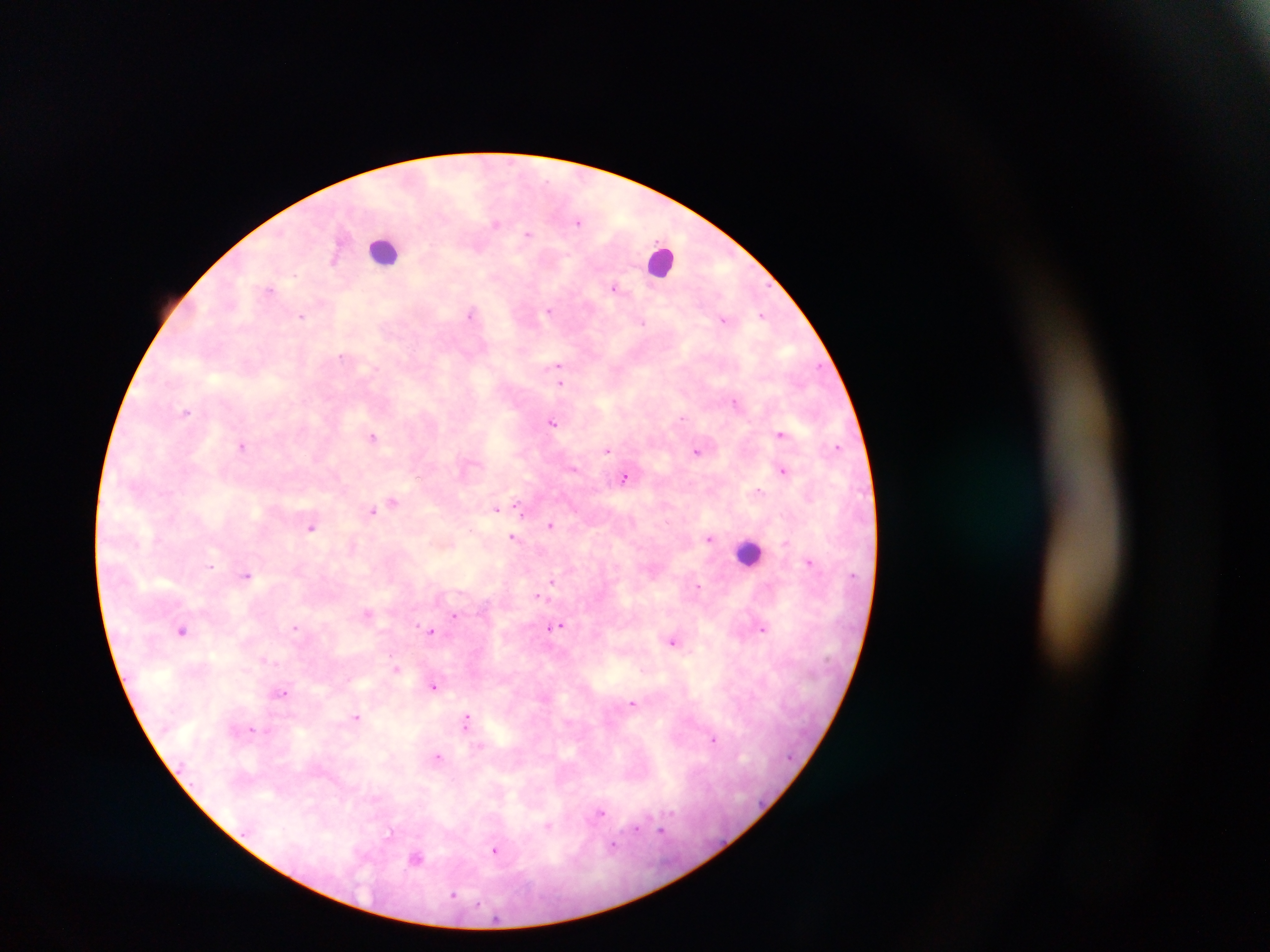 Approximate centers as (x, y) in pixels. Leukocyte locations: (384, 250), (663, 261), (748, 552). Plasmodium parasite locations: (579, 222), (495, 224), (528, 234), (479, 248), (333, 258), (614, 287), (270, 288), (549, 310), (471, 314), (762, 315), (302, 317), (724, 320), (643, 323), (342, 356), (558, 365), (561, 384), (735, 402), (186, 413), (682, 418), (552, 422), (780, 433), (372, 436), (242, 447), (837, 447), (607, 450), (697, 452), (573, 469), (784, 470), (625, 477), (758, 492), (393, 502), (518, 507), (495, 509), (372, 511), (550, 525), (311, 527), (512, 537), (709, 539), (784, 543), (809, 561), (210, 566), (246, 574), (552, 582), (698, 587), (539, 596), (368, 614), (454, 616), (559, 626), (295, 627), (763, 629), (182, 630), (430, 631), (673, 641), (396, 668), (434, 686), (281, 694), (633, 703), (357, 717), (467, 720), (251, 729), (714, 740), (438, 757), (599, 813), (548, 826), (636, 828), (661, 830), (390, 831), (613, 846), (495, 851), (416, 859), (453, 895). Thick blood smear. Sample from Ghana. Single field of view. Image is 1270×952 pixels. Photographed through a microscope with a mobile-phone camera.